Report the malaria status.
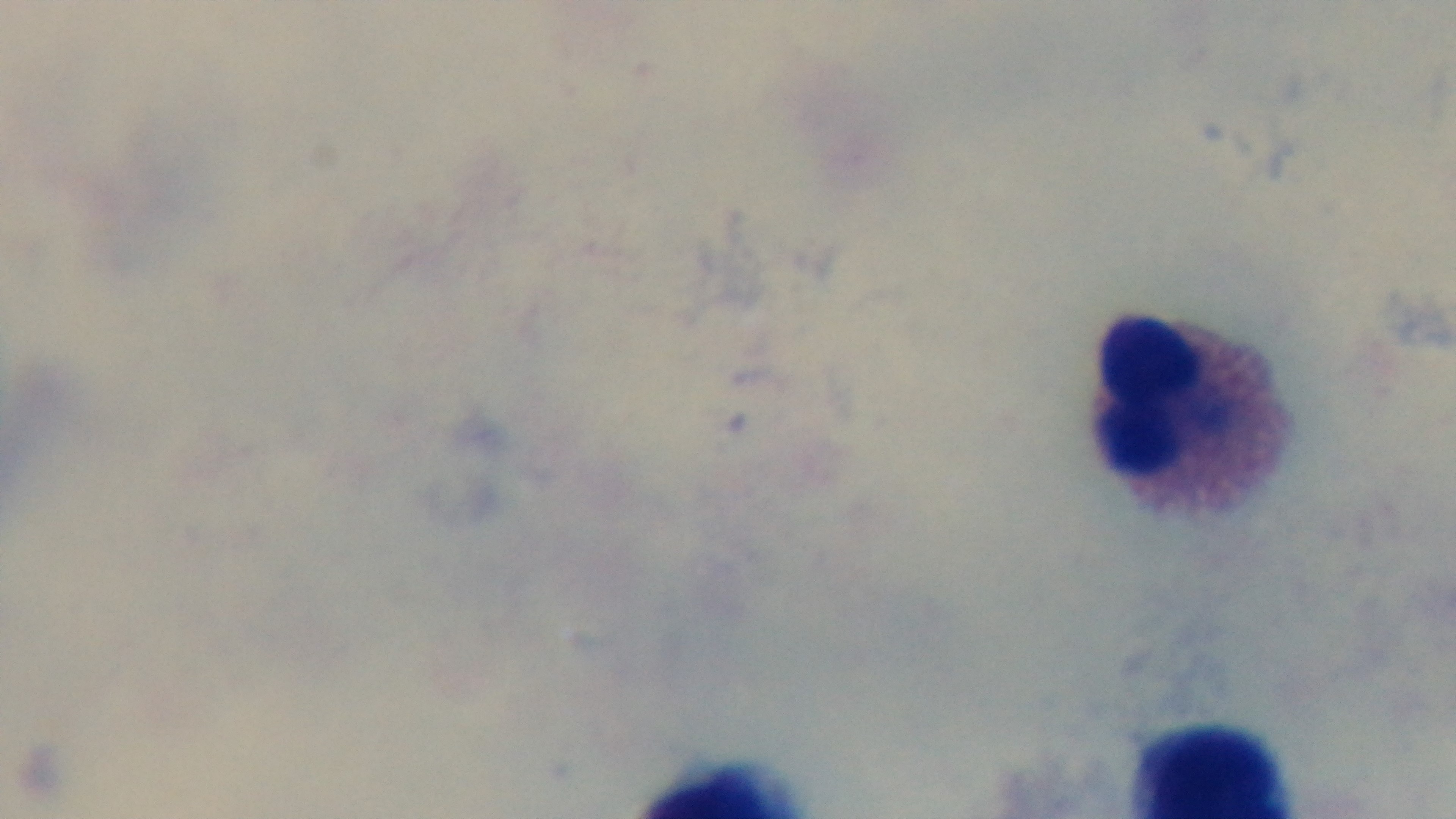
Uninfected.

Summary:
  - Objective: 100x oil immersion
  - Field of view: one from the slide
  - Stain: Giemsa
  - Capture: mounted 4K digital camera
  - Modality: light microscopy
  - Preparation: thick smear